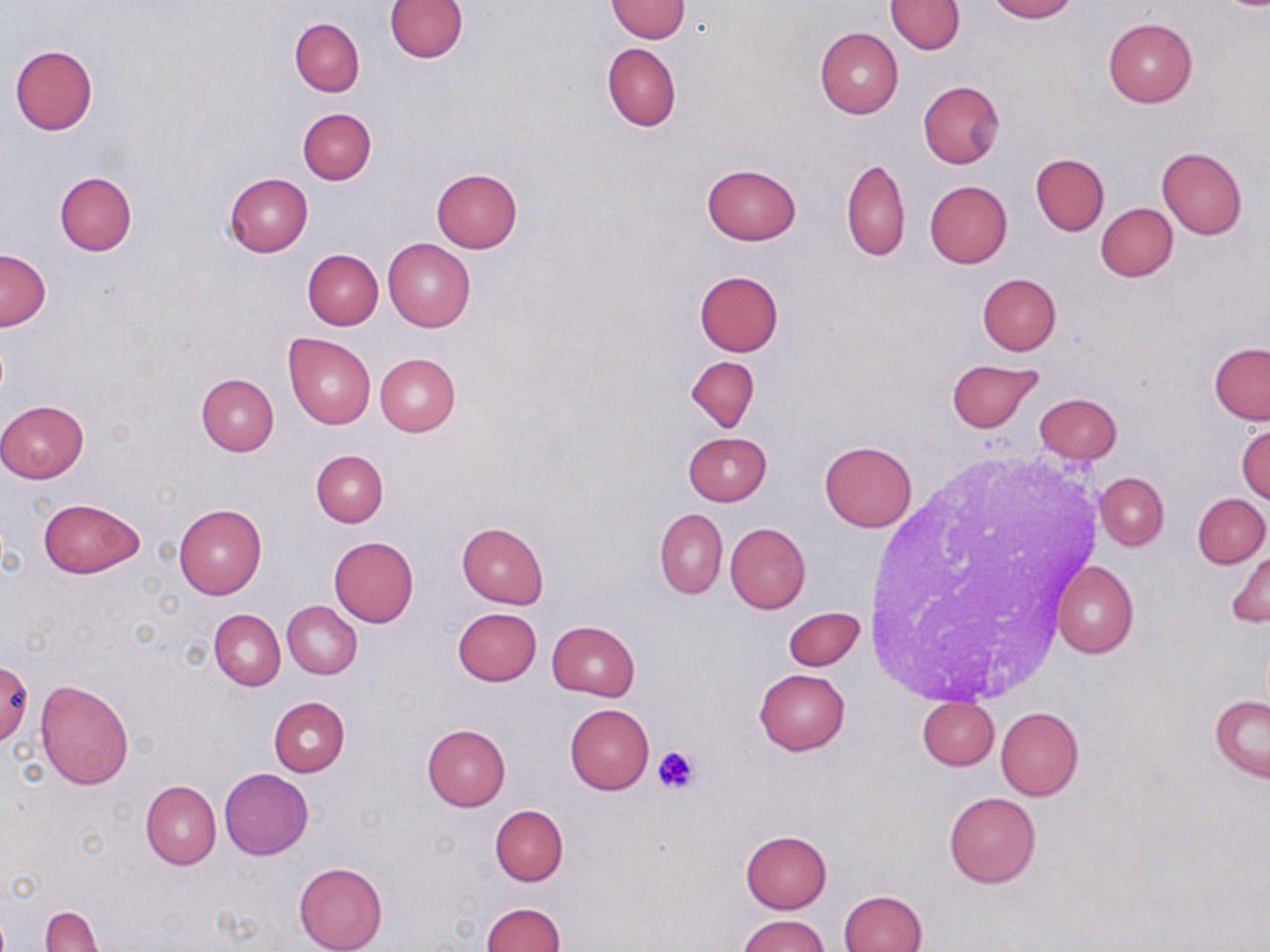
slide_level_diagnosis: negative for blood parasites
magnification: 1000x
modality: optical microscopy
platelet_locations: 'approximate bounding boxes as (x1,y1)-(x2,y2) corner pairs in pixels: (651,746)-(700,796)'
uninfected_red_blood_cell_locations: 'approximate bounding boxes as (x1,y1)-(x2,y2) corner pairs in pixels: (385,0)-(469,62), (606,0)-(691,43), (987,0)-(1077,22), (885,1)-(965,53), (1102,17)-(1197,108), (290,18)-(365,97), (814,27)-(903,119), (602,42)-(681,132), (9,45)-(98,135), (918,81)-(1004,168), (298,108)-(376,184), (1157,147)-(1247,240), (1030,153)-(1109,235), (841,157)-(911,261), (702,162)-(801,244), (432,169)-(523,253), (54,173)-(136,255), (223,173)-(313,257), (924,180)-(1013,268), (1095,204)-(1177,281), (383,238)-(475,332), (0,248)-(50,330), (303,249)-(383,329), (693,270)-(784,356), (977,273)-(1061,354), (283,332)-(375,429), (1209,343)-(1270,423), (375,352)-(460,436), (686,356)-(759,432), (946,359)-(1043,433), (196,373)-(279,455), (1035,393)-(1122,464), (0,400)-(89,482), (1236,423)-(1270,504), (683,432)-(771,506), (820,440)-(917,533), (311,450)-(388,526), (1095,472)-(1168,550), (1193,493)-(1269,567), (38,498)-(145,578), (175,504)-(265,599), (655,507)-(727,600), (725,522)-(810,613), (457,523)-(549,608), (329,536)-(419,627), (1228,547)-(1270,628), (1051,559)-(1138,658), (284,601)-(362,678), (453,608)-(541,686), (783,608)-(863,671), (210,609)-(286,690), (547,620)-(640,701), (2,660)-(33,744), (753,669)-(850,755), (35,679)-(134,789), (1210,695)-(1269,780), (269,696)-(350,777), (917,697)-(998,770), (564,704)-(653,794), (995,707)-(1084,801), (422,724)-(510,810), (219,769)-(313,859), (141,780)-(220,870), (943,792)-(1041,888), (490,805)-(568,886), (739,829)-(832,914), (294,861)-(387,952), (838,890)-(928,952), (479,902)-(564,952), (40,907)-(103,952), (737,914)-(831,952)'
field_of_view: single
stain: May-Grünwald-Giemsa
image_size: 1270×952 pixels
preparation: thin blood smear